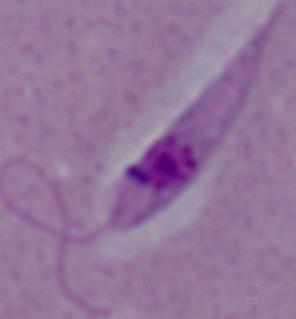

Captured at 1000x magnification. A Leishmania parasite is shown. Photomicrograph.